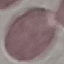

Summary:
  - Result: no malaria parasites detected
  - Capture: smartphone through the microscope eyepiece
  - Preparation: thin smear
  - Image type: automatically extracted cell patch, resized to 64 × 64 pixels
  - Stain: Giemsa